State which parasite is depicted.
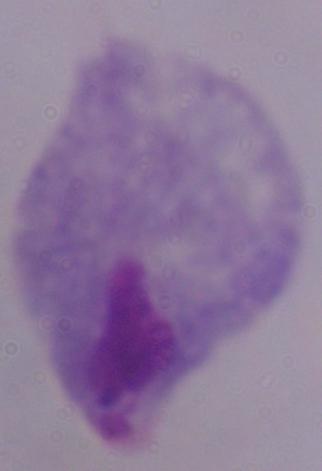

A trichomonad.

{
  "magnification": "1000x",
  "modality": "micrograph"
}